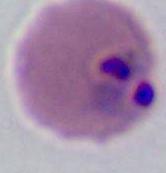

Micrograph. Captured at either 400x or 1000x magnification. A Plasmodium parasite is seen.